Assess this cell for malaria.
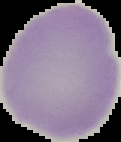
It is uninfected.

Summary:
  - Image type: cell region segmented out of the field of view; surrounding area masked to black
  - Preparation: thin blood film
  - Image size: 121×142 pixels